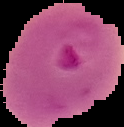 Result: malaria parasites identified. From a thin blood film. Cell region segmented out of the field of view; the surrounding area is masked to black. Image is 124×127 pixels.